Identify the cell.
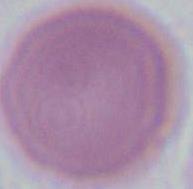

This is an erythrocyte.

Summary:
  - Modality: micrograph
  - Magnification: 1000x